Identify the parasite.
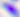

This is Toxoplasma gondii.

{
  "modality": "micrograph",
  "magnification": "400x"
}